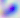

Micrograph. Toxoplasma gondii is shown. 400x magnification.